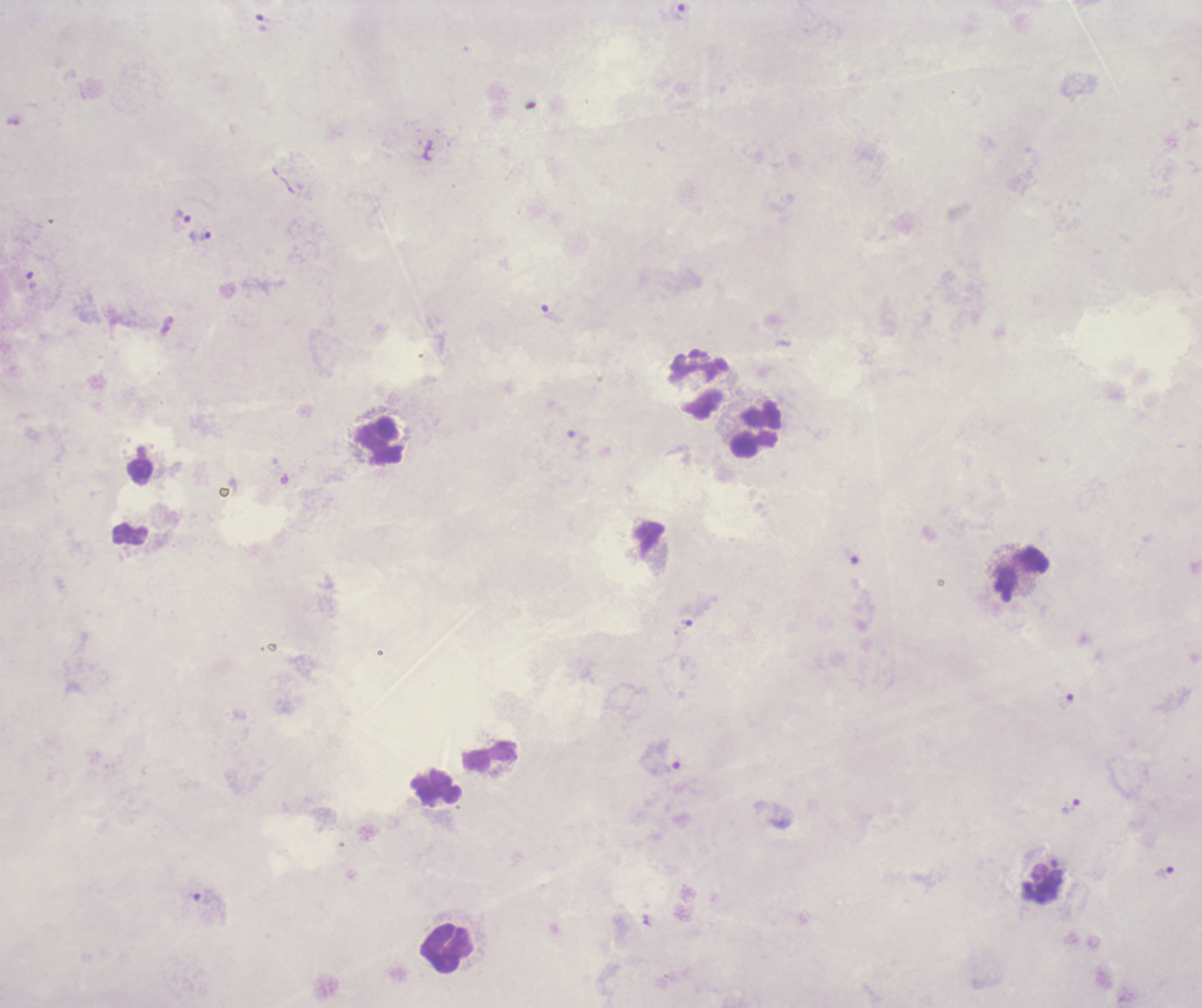
Approximate centers as [x, y] in pixels. Trophozoite locations: [680, 12], [268, 22], [182, 219], [200, 238], [552, 315], [579, 440], [1067, 702], [660, 758], [1071, 807], [1164, 873]. Leukocyte locations: [698, 388], [758, 431], [379, 441], [141, 471], [1022, 575], [490, 755], [437, 787], [1043, 885], [447, 947]. Single field of view. Background quality: unsatisfactory. Romanowsky-stained preparation. Coloration quality: bad. Result: positive for malaria parasites. Previously used in an actual diagnosis. Image is 1202×1008 pixels. Thick blood smear. 100x magnification.